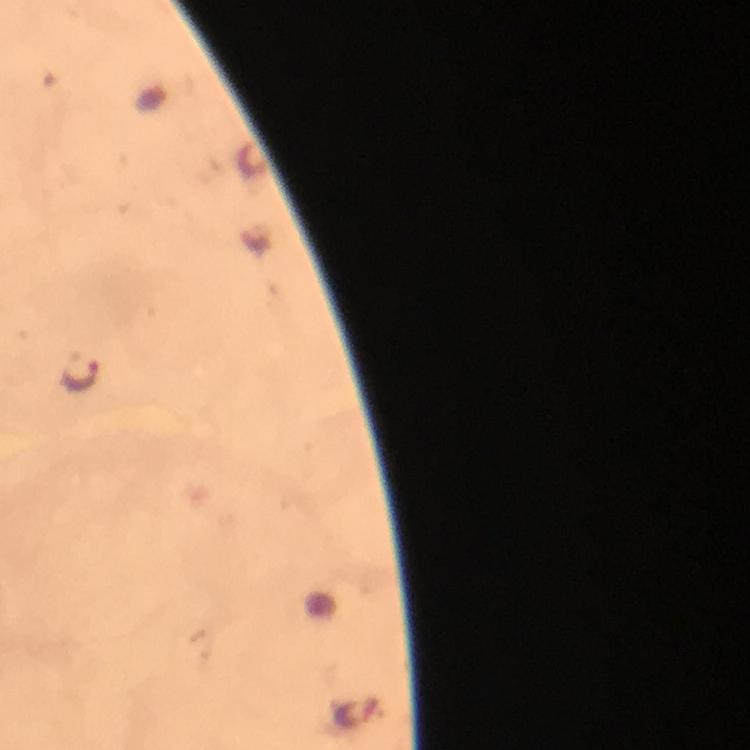
malaria parasite locations = approximate centers as {x, y} in pixels: {80, 375}
cropped from = one field of view
capture = smartphone camera through the microscope
context = from a malaria diagnostic workup
immersion oil = applied
stain = Giemsa
preparation = thick blood smear
magnification = 100x
image size = 750×750 pixels